Give the preparation type.
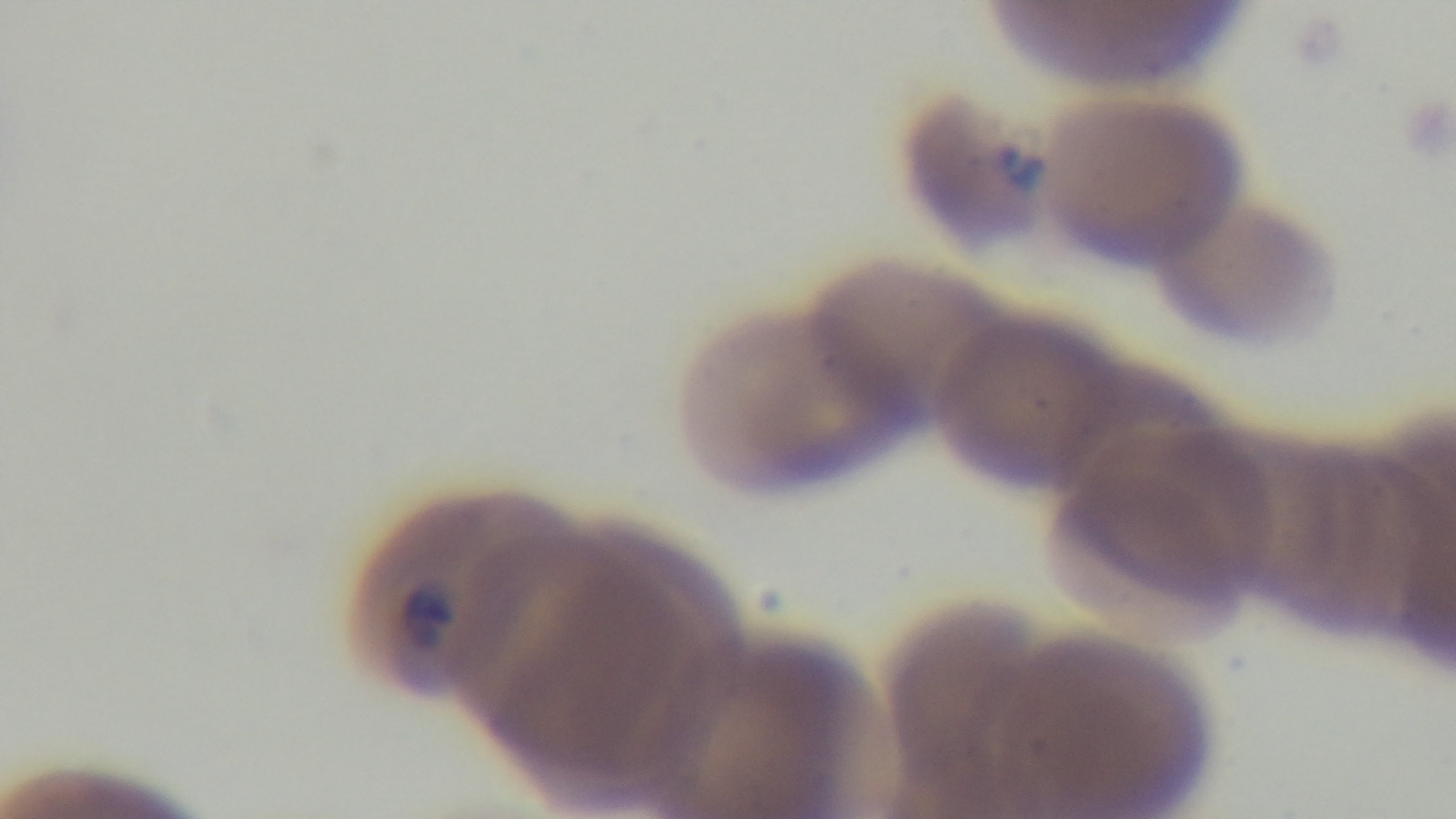

A thin smear.

Summary:
  - Malaria status: infected
  - Modality: light microscopy
  - Field of view: single
  - Capture: mounted 4K digital camera
  - Objective: 100x oil immersion
  - Stain: Giemsa